Outline each blood parasite and name the species.
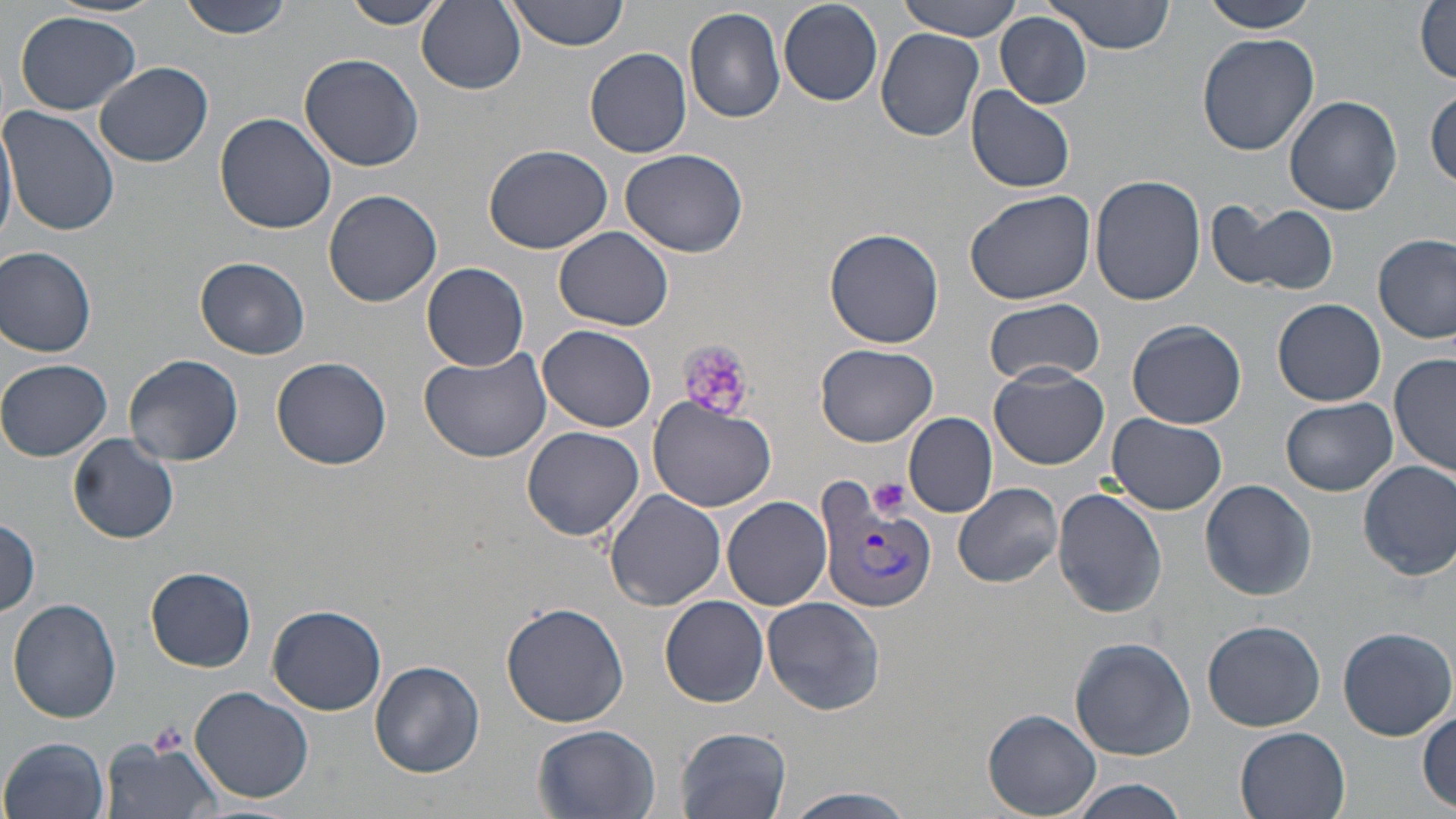
Approximate bounding boxes as [x1, y1, x2, y2] in pixels.
Plasmodium vivax-infected red blood cells: [814, 477, 938, 617].
No Plasmodium falciparum, Plasmodium ovale, Plasmodium malariae, Babesia divergens, or Trypanosoma brucei observed.

Summary:
  - Platelet locations: [678, 339, 754, 423], [868, 477, 911, 521], [146, 718, 191, 758]
  - Uninfected red blood cell locations: [177, 0, 296, 40], [339, 0, 448, 28], [417, 0, 527, 94], [502, 0, 628, 51], [896, 0, 1024, 40], [1043, 0, 1174, 54], [1202, 0, 1319, 33], [778, 2, 883, 104], [1415, 2, 1455, 84], [683, 8, 786, 125], [14, 11, 141, 115], [995, 12, 1092, 109], [877, 29, 984, 141], [1197, 33, 1320, 155], [586, 47, 692, 158], [298, 53, 424, 171], [95, 61, 213, 167], [967, 88, 1075, 194], [1427, 90, 1456, 187], [1284, 95, 1402, 215], [1, 106, 120, 237], [0, 111, 17, 248], [215, 112, 337, 234], [484, 144, 613, 255], [621, 147, 748, 257], [1091, 174, 1208, 305], [324, 189, 442, 307], [965, 190, 1096, 307], [1212, 199, 1341, 296], [554, 225, 674, 330], [824, 227, 946, 349], [1374, 234, 1455, 343], [1, 246, 99, 357], [195, 256, 310, 359], [421, 261, 529, 370], [1274, 297, 1385, 406], [985, 299, 1105, 385], [1127, 319, 1246, 429], [536, 324, 656, 432], [816, 344, 938, 448], [417, 345, 550, 462], [1390, 354, 1454, 479], [122, 355, 243, 466], [271, 356, 392, 470], [1, 359, 112, 460], [991, 365, 1109, 469], [648, 396, 779, 512], [1280, 397, 1397, 496], [904, 412, 997, 516], [1107, 414, 1228, 515], [520, 425, 644, 541], [69, 434, 179, 543], [1357, 459, 1456, 579], [1200, 478, 1317, 601], [954, 482, 1063, 587], [1053, 487, 1167, 616], [605, 490, 727, 609], [722, 495, 831, 609], [0, 519, 42, 616], [146, 567, 256, 671], [661, 595, 769, 707], [761, 595, 885, 715], [7, 598, 122, 723], [502, 601, 629, 727], [266, 604, 386, 715], [1203, 620, 1325, 729], [1336, 625, 1456, 740], [1068, 635, 1196, 760], [372, 660, 484, 777], [189, 687, 314, 802], [1416, 707, 1455, 808], [984, 708, 1102, 817], [532, 726, 661, 818], [1235, 726, 1351, 819], [675, 728, 792, 819], [2, 735, 108, 818], [102, 738, 224, 819], [1064, 778, 1190, 819], [783, 786, 920, 818]
  - Slide-level diagnosis: Plasmodium vivax
  - Field of view: single
  - Image size: 1456×819 pixels
  - Modality: light microscopy
  - Stain: May-Grünwald-Giemsa
  - Magnification: 1000x
  - Preparation: thin blood smear